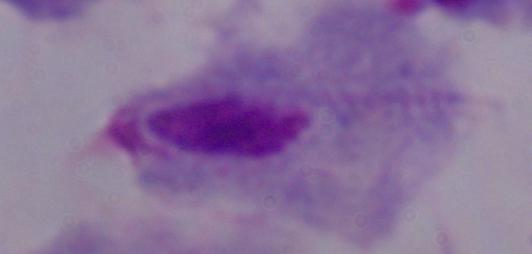

Summary:
  - Modality: photomicrograph
  - Identification: trichomonad
  - Magnification: 1000x